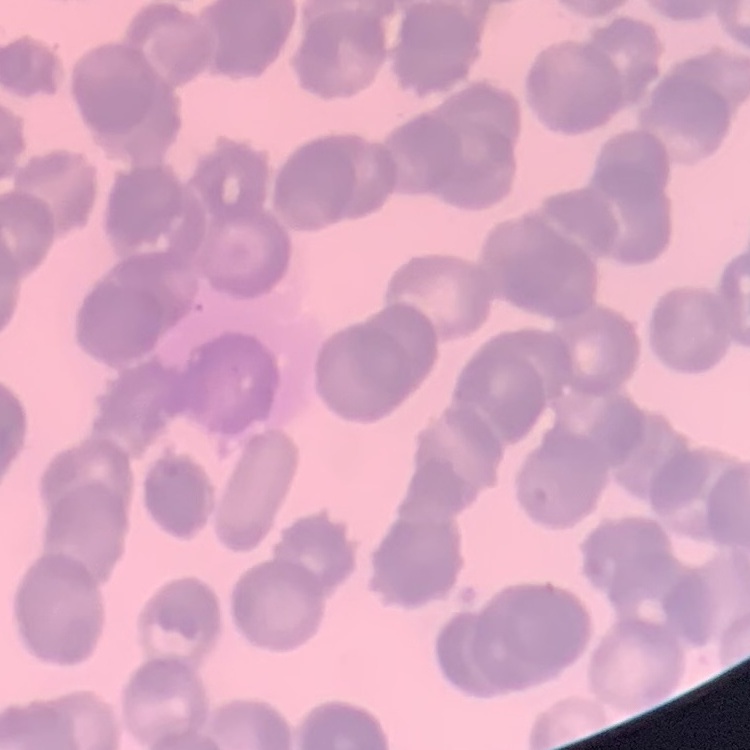

Summary:
  - Red blood cell morphology: rouleaux formation
  - Image type: square crop of a larger photomicrograph
  - Stain: Field's or Giemsa
  - Preparation: thin blood film